Name the parasite shown.
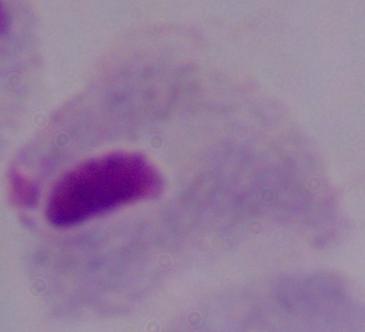

A trichomonad.

Summary:
  - Modality: photomicrograph
  - Magnification: 1000x